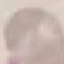

Summary:
  - Malaria status: uninfected
  - Stain: Giemsa
  - Capture: smartphone camera at the microscope eyepiece
  - Preparation: thin smear
  - Image type: automatically extracted cell patch, resized to 64 × 64 pixels